Outline each Plasmodium falciparum-infected red blood cell.
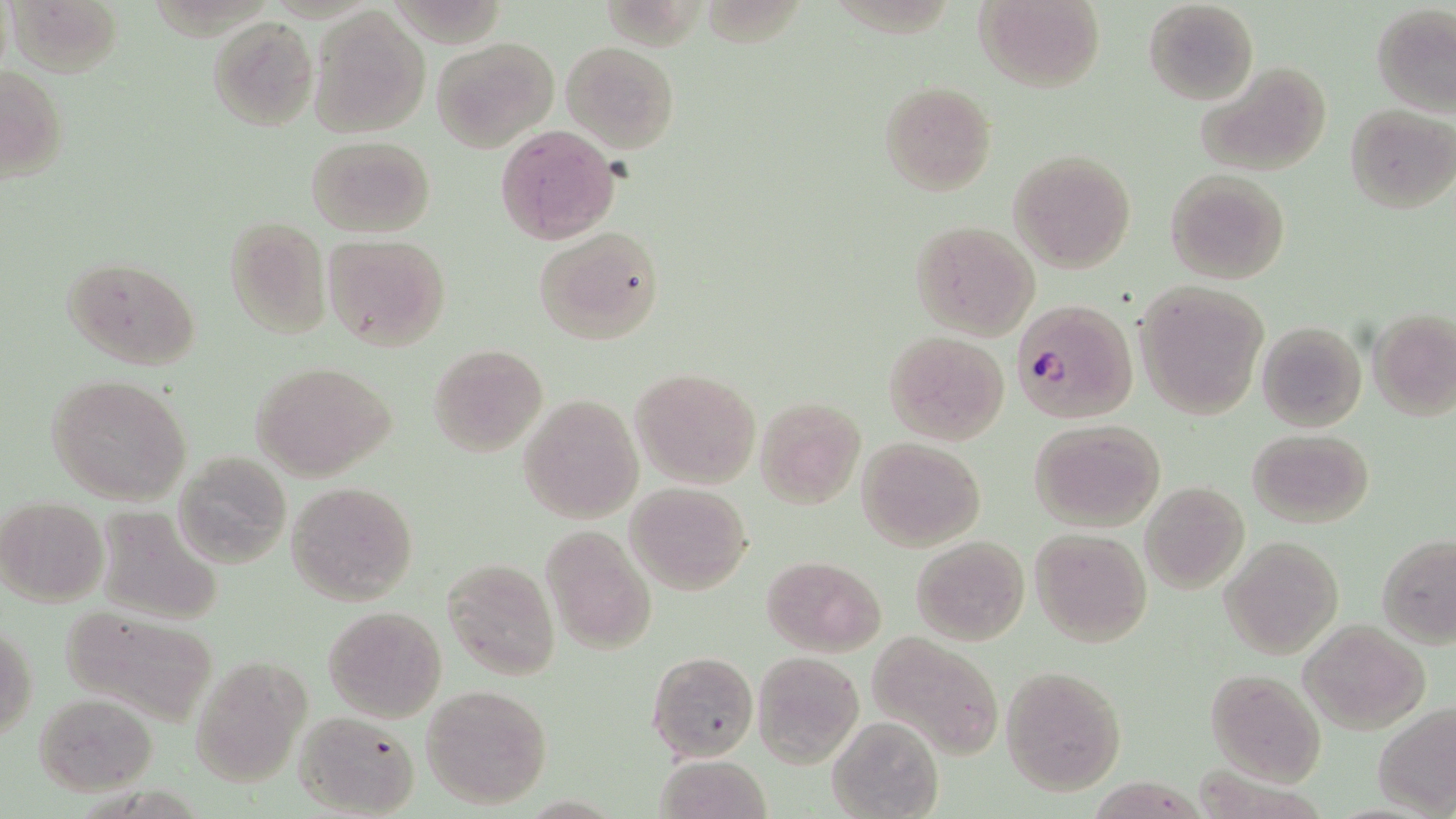

Approximate bounding boxes as named x1/y1/x2/y2 corners in pixels.
Plasmodium falciparum-infected red blood cells: (x1=1010, y1=299, x2=1138, y2=425).

{
  "slide_level_diagnosis": "Plasmodium falciparum",
  "magnification": "1000x",
  "uninfected_red_blood_cell_locations": "approximate bounding boxes as named x1/y1/x2/y2 corners in pixels: (x1=6, y1=0, x2=123, y2=79), (x1=973, y1=0, x2=1104, y2=91), (x1=1143, y1=0, x2=1259, y2=104), (x1=1372, y1=3, x2=1456, y2=116), (x1=308, y1=5, x2=432, y2=139), (x1=208, y1=15, x2=319, y2=130), (x1=431, y1=35, x2=559, y2=154), (x1=561, y1=41, x2=680, y2=153), (x1=1195, y1=61, x2=1334, y2=177), (x1=0, y1=65, x2=69, y2=183), (x1=878, y1=80, x2=996, y2=197), (x1=1345, y1=104, x2=1455, y2=212), (x1=494, y1=125, x2=622, y2=244), (x1=306, y1=135, x2=435, y2=237), (x1=1010, y1=149, x2=1135, y2=273), (x1=1165, y1=170, x2=1291, y2=284), (x1=223, y1=217, x2=331, y2=341), (x1=908, y1=220, x2=1040, y2=341), (x1=535, y1=227, x2=664, y2=346), (x1=324, y1=236, x2=451, y2=353), (x1=62, y1=256, x2=201, y2=371), (x1=1135, y1=281, x2=1269, y2=420), (x1=1368, y1=308, x2=1456, y2=421), (x1=1256, y1=320, x2=1367, y2=433), (x1=883, y1=331, x2=1010, y2=445), (x1=428, y1=343, x2=547, y2=458), (x1=250, y1=360, x2=396, y2=482), (x1=631, y1=367, x2=761, y2=491), (x1=47, y1=373, x2=191, y2=506), (x1=518, y1=393, x2=644, y2=523), (x1=755, y1=397, x2=865, y2=509), (x1=1030, y1=418, x2=1167, y2=531), (x1=1246, y1=428, x2=1375, y2=527), (x1=857, y1=438, x2=985, y2=551), (x1=173, y1=452, x2=294, y2=567), (x1=286, y1=481, x2=418, y2=605), (x1=625, y1=482, x2=753, y2=595), (x1=1140, y1=482, x2=1249, y2=596), (x1=1, y1=496, x2=108, y2=607), (x1=94, y1=508, x2=224, y2=625), (x1=543, y1=526, x2=658, y2=654), (x1=1029, y1=527, x2=1152, y2=647), (x1=912, y1=535, x2=1030, y2=646), (x1=1376, y1=535, x2=1456, y2=648), (x1=1221, y1=537, x2=1343, y2=659), (x1=762, y1=555, x2=887, y2=656), (x1=443, y1=558, x2=559, y2=680), (x1=55, y1=605, x2=224, y2=725), (x1=323, y1=606, x2=447, y2=723), (x1=1300, y1=618, x2=1429, y2=733), (x1=1, y1=622, x2=37, y2=741), (x1=868, y1=632, x2=1002, y2=760), (x1=646, y1=649, x2=760, y2=763), (x1=753, y1=653, x2=863, y2=765), (x1=188, y1=657, x2=310, y2=789), (x1=1001, y1=665, x2=1126, y2=794), (x1=1204, y1=670, x2=1324, y2=785), (x1=420, y1=684, x2=554, y2=810), (x1=32, y1=691, x2=159, y2=795), (x1=1373, y1=703, x2=1456, y2=816), (x1=292, y1=711, x2=419, y2=818), (x1=828, y1=715, x2=942, y2=819), (x1=654, y1=753, x2=772, y2=819)",
  "preparation": "thin blood film",
  "field_of_view": "single",
  "stain": "May-Grünwald-Giemsa",
  "modality": "light microscopy",
  "image_size": "1456×819 pixels"
}